State which parasite is depicted.
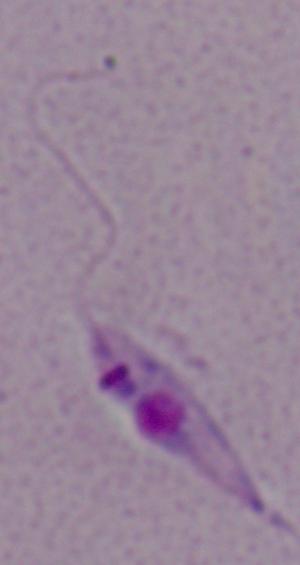
Leishmania.

Photomicrograph. Captured at 1000x magnification.